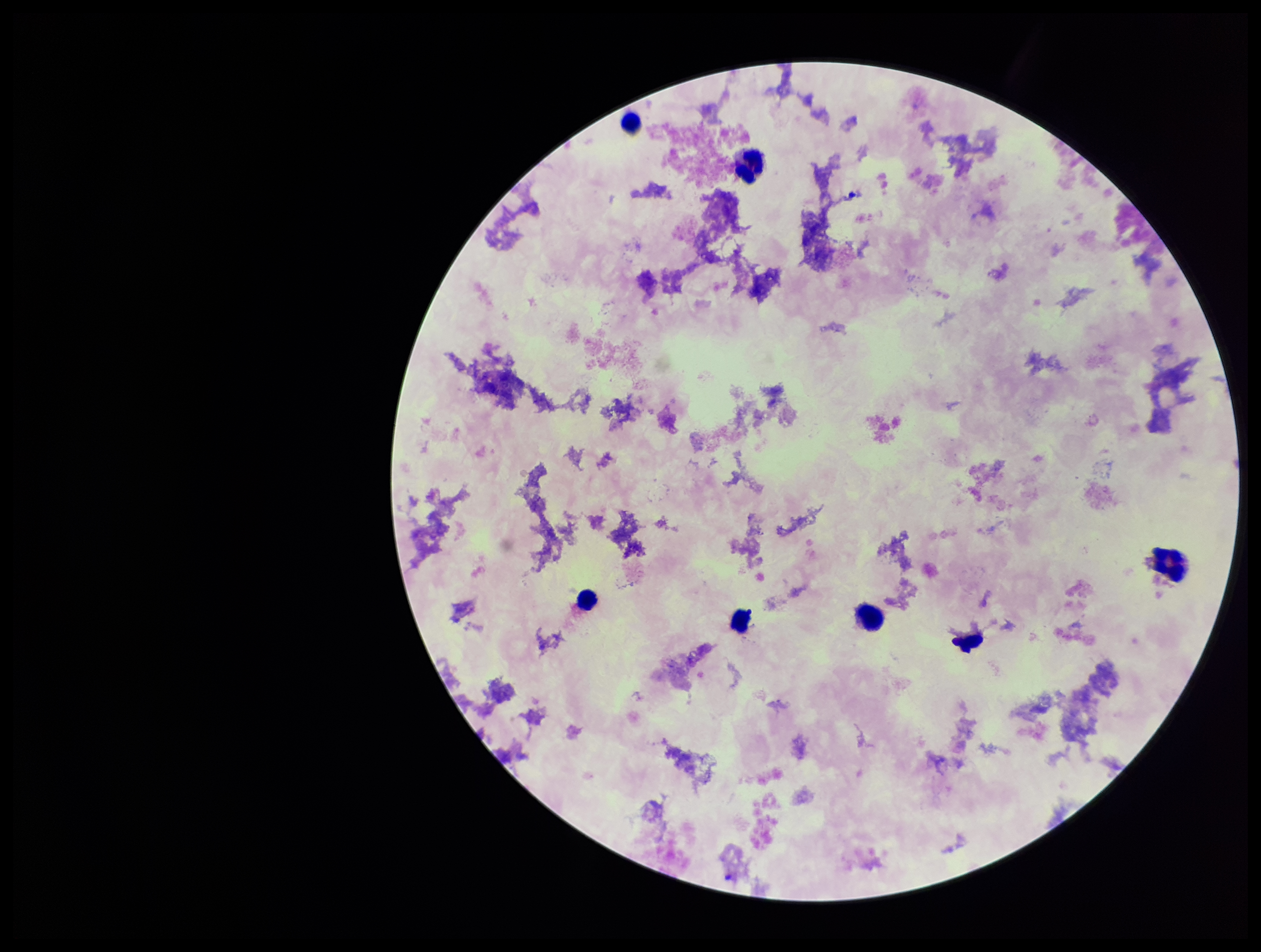

{
  "plasmodium_parasites": "none identified",
  "patient_malaria_status": "negative",
  "field_of_view": "single",
  "parasite_count": 0,
  "capture": "smartphone photograph through the microscope eyepiece",
  "stain": "Giemsa",
  "image_size": "1261×952 pixels",
  "leukocyte_count": 7,
  "preparation": "thick smear"
}